Point out each leukocyte.
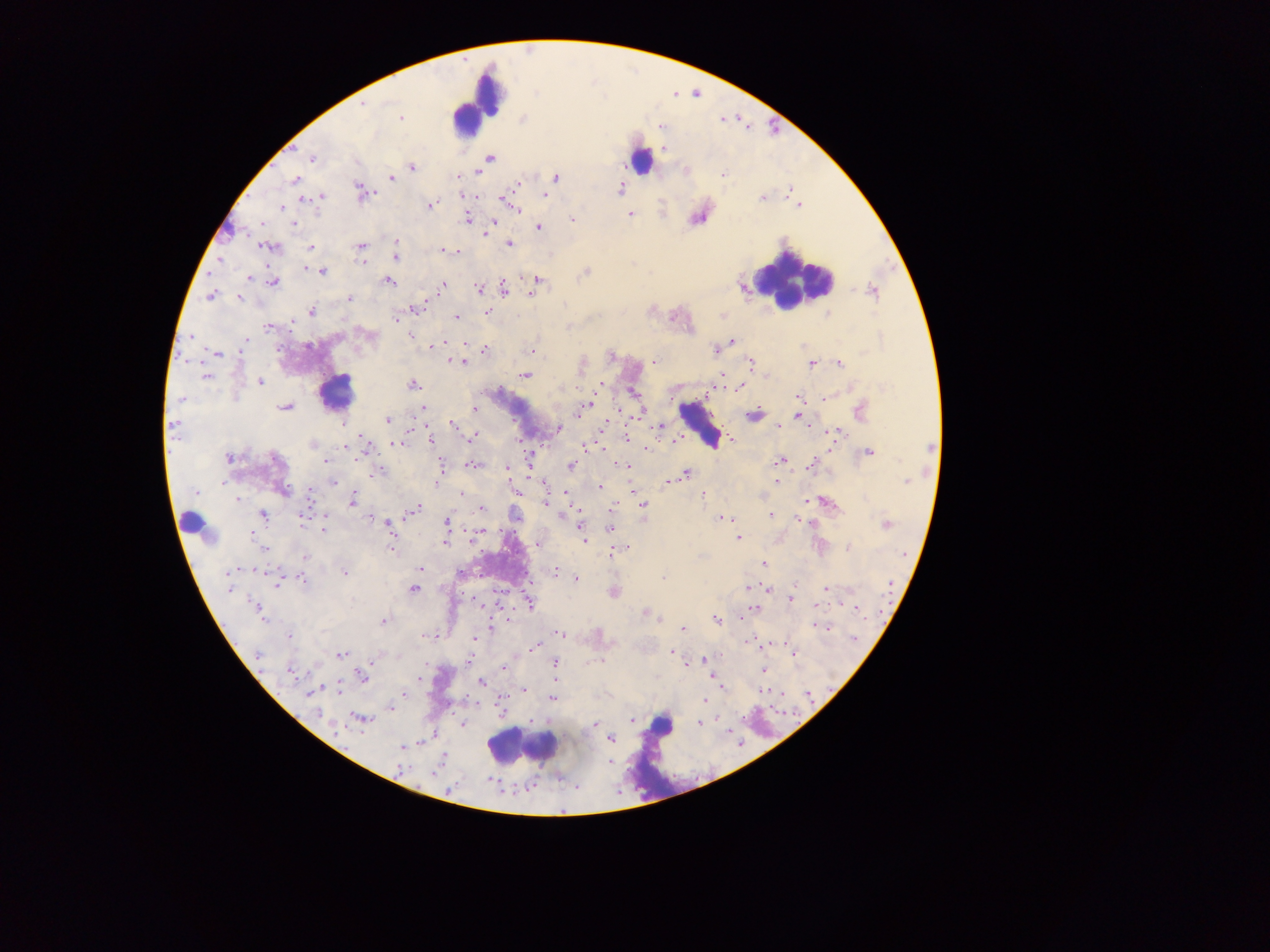

Approximate centers as [x, y] in pixels.
Leukocytes (some below the resolvable threshold): [478, 104], [643, 157], [791, 279], [335, 392], [699, 424], [191, 523], [661, 726], [521, 746].

Plasmodium parasite locations: [363, 104], [400, 118], [312, 158], [489, 158], [412, 167], [723, 175], [457, 177], [392, 178], [556, 178], [295, 180], [516, 185], [621, 189], [362, 193], [545, 195], [322, 197], [313, 198], [763, 198], [304, 201], [506, 201], [513, 205], [798, 205], [431, 206], [282, 207], [630, 214], [467, 219], [573, 219], [293, 224], [490, 224], [539, 228], [397, 244], [509, 244], [361, 246], [269, 247], [311, 248], [443, 251], [457, 251], [396, 257], [220, 260], [361, 262], [322, 272], [586, 272], [249, 279], [538, 280], [273, 282], [389, 282], [535, 285], [442, 286], [479, 288], [504, 289], [872, 291], [211, 294], [239, 297], [350, 299], [417, 308], [312, 311], [487, 312], [456, 317], [396, 319], [292, 322], [267, 327], [370, 335], [411, 335], [190, 337], [246, 339], [732, 341], [245, 343], [442, 343], [433, 345], [278, 350], [484, 350], [716, 350], [532, 351], [217, 354], [654, 360], [463, 362], [749, 363], [839, 363], [811, 364], [525, 375], [722, 376], [206, 378], [260, 381], [413, 384], [599, 385], [740, 386], [798, 396], [182, 398], [825, 398], [585, 407], [285, 408], [422, 408], [474, 409], [580, 411], [860, 411], [753, 414], [801, 416], [387, 420], [173, 425], [453, 425], [604, 426], [660, 426], [559, 428], [835, 433], [627, 436], [473, 437], [362, 440], [431, 440], [733, 440], [675, 441], [313, 444], [395, 444], [344, 447], [585, 448], [646, 448], [869, 452], [229, 459], [275, 459], [325, 461], [779, 461], [472, 464], [811, 465], [570, 466], [626, 466], [441, 468], [507, 468], [379, 471], [685, 474], [670, 481], [906, 481], [333, 482], [776, 482], [223, 483], [545, 483], [600, 486], [283, 491], [196, 492], [567, 493], [462, 494], [702, 494], [310, 496], [238, 499], [351, 502], [827, 502], [546, 504], [643, 506], [614, 507], [416, 508], [481, 508], [412, 511], [262, 515], [771, 515], [720, 518], [729, 519], [302, 520], [388, 523], [447, 524], [887, 525], [579, 526], [323, 528], [610, 528], [251, 533], [478, 533], [739, 538], [583, 540], [445, 541], [264, 547], [390, 547], [614, 551], [306, 557], [763, 564], [419, 568], [230, 572], [554, 572], [344, 573], [663, 577], [575, 579], [303, 580], [277, 582], [795, 584], [827, 588], [228, 589], [413, 589], [766, 589], [790, 600], [529, 603], [258, 608], [753, 609], [857, 609], [260, 613], [647, 614], [716, 619], [383, 620], [491, 627], [825, 627], [682, 628], [560, 634], [289, 636], [425, 636], [854, 639], [475, 640], [535, 646], [671, 652], [341, 654], [257, 655], [794, 655], [705, 660], [600, 661], [688, 664], [555, 665], [504, 668], [764, 669], [291, 672], [361, 676], [713, 678], [420, 679], [481, 682], [338, 689], [525, 690], [313, 691], [403, 694], [552, 698], [704, 700], [391, 707], [319, 714], [360, 719], [632, 720], [699, 723], [594, 725], [610, 739], [402, 746]. Sample from Ghana. Thick blood smear. Image is 1270×952 pixels. Photographed through a microscope with a mobile-phone camera. Single field of view.